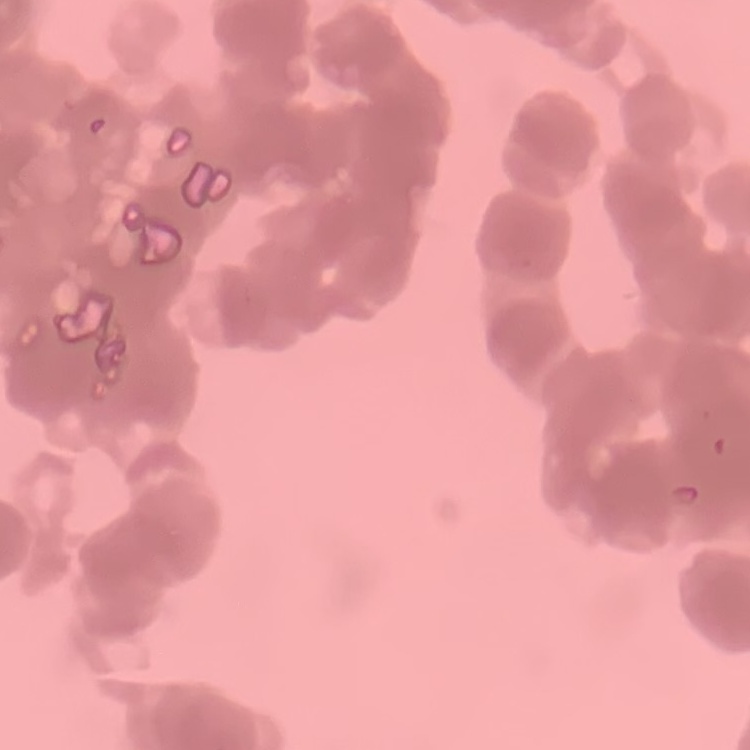

The erythrocytes show rouleaux formation. Thin peripheral smear. Square crop of a larger photomicrograph. Field's or Giemsa stain.